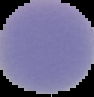
From a thin blood film. Image is 94×97 pixels. Cell region segmented out of the field of view; the surrounding area is masked to black. Malaria status: uninfected.